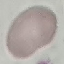

{
  "result": "negative for malaria parasites",
  "preparation": "thin blood smear",
  "image_type": "automatically extracted cell patch, resized to 64 × 64 pixels",
  "capture": "smartphone camera at the microscope eyepiece",
  "stain": "Giemsa"
}